Identify the parasite.
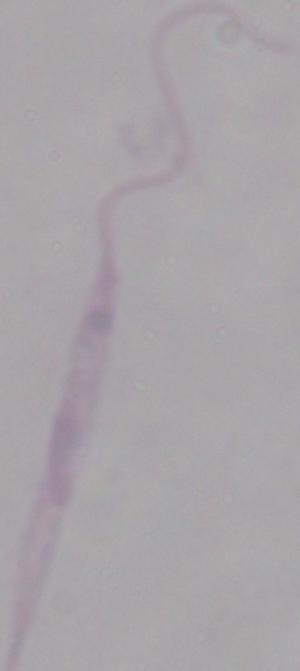

This is Leishmania.

Photomicrograph. Captured at 1000x magnification.